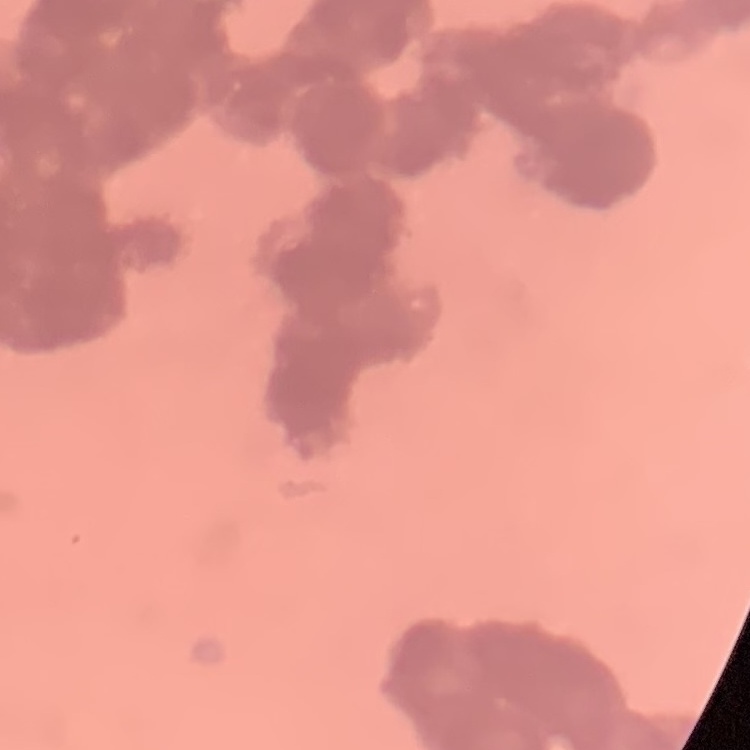

Summary:
  - Red blood cell morphology: rouleaux formation
  - Image type: square crop of a larger photomicrograph
  - Preparation: thin blood smear
  - Stain: Field's or Giemsa